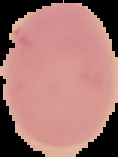
Summary:
  - Result: no Plasmodium parasites seen
  - Image type: cell region segmented out of the field of view; surrounding area masked to black
  - Image size: 118×157 pixels
  - Preparation: thin blood film